Locate every blood parasite and identify its species.
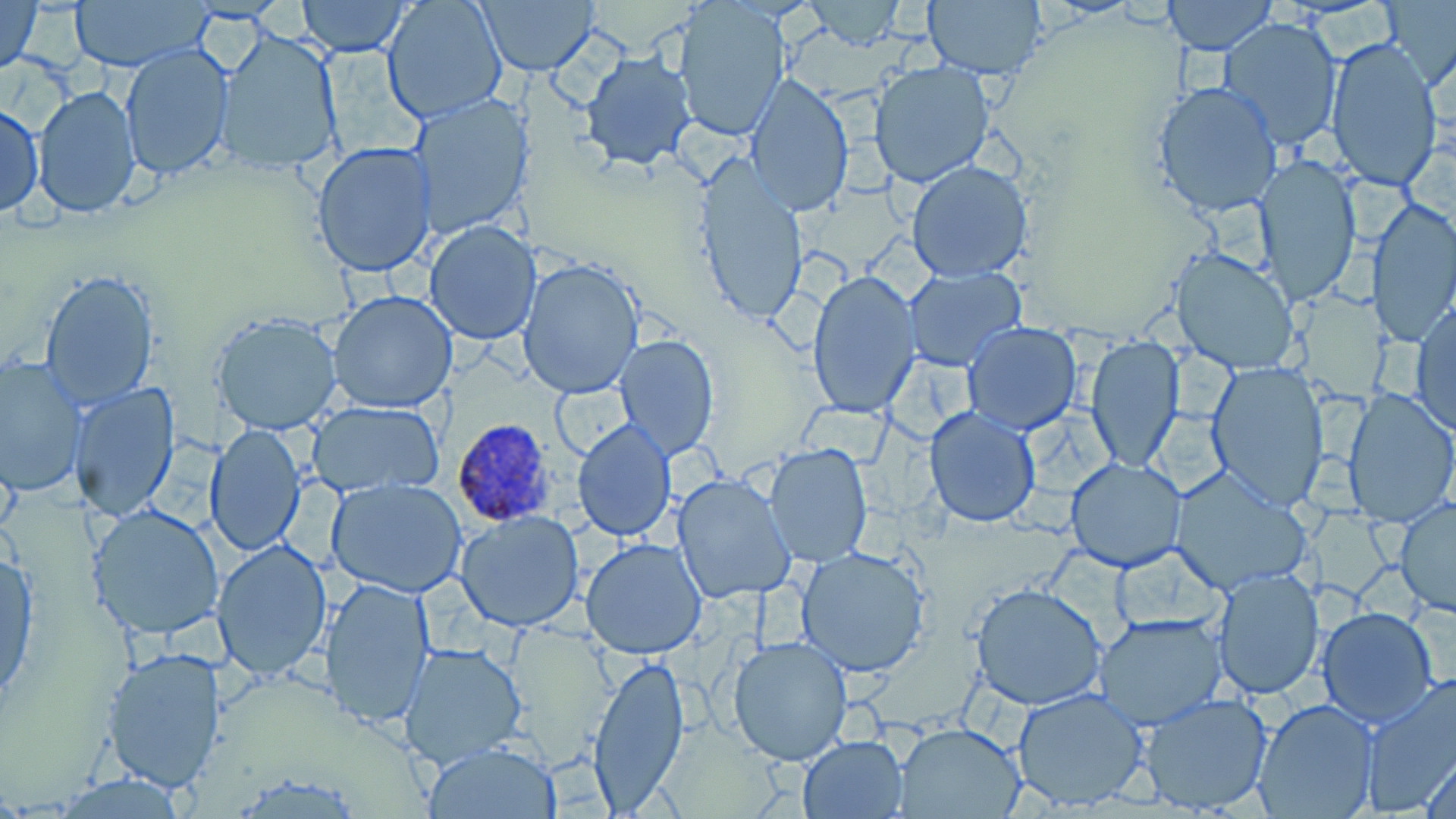
Approximate bounding boxes as (x1,y1)-(x2,y2) corner pairs in pixels.
Plasmodium ovale-infected red blood cells: (450,417)-(556,523).
No Plasmodium falciparum, Plasmodium malariae, Plasmodium vivax, Babesia divergens, or Trypanosoma brucei observed.

Summary:
  - Uninfected red blood cell locations: (0,0)-(45,76), (67,0)-(214,72), (295,0)-(412,56), (380,0)-(510,123), (795,0)-(916,53), (922,0)-(1048,82), (1164,0)-(1278,55), (477,1)-(600,78), (670,1)-(794,141), (1379,1)-(1456,87), (1214,16)-(1343,149), (216,29)-(343,176), (1324,37)-(1444,193), (119,43)-(233,178), (582,52)-(698,170), (870,61)-(995,187), (743,74)-(854,216), (1152,82)-(1284,220), (31,86)-(142,217), (410,95)-(534,239), (1,102)-(45,217), (310,142)-(438,277), (689,155)-(807,327), (1250,156)-(1363,304), (905,160)-(1034,281), (1367,195)-(1456,350), (426,220)-(541,346), (1171,247)-(1299,374), (517,259)-(645,400), (905,267)-(1025,370), (40,268)-(161,407), (808,270)-(921,419), (328,289)-(458,412), (1411,299)-(1456,437), (213,311)-(345,436), (962,322)-(1081,435), (614,333)-(719,459), (1085,337)-(1184,472), (0,356)-(85,498), (1205,361)-(1329,511), (70,383)-(181,523), (1340,388)-(1456,528), (306,400)-(445,495), (924,406)-(1041,528), (572,419)-(676,540), (206,423)-(307,557), (764,444)-(875,568), (1065,457)-(1186,572), (1169,467)-(1314,595), (671,473)-(797,606), (327,479)-(468,598), (1394,499)-(1456,614), (89,503)-(226,640), (454,511)-(586,630), (212,538)-(333,680), (581,538)-(709,660), (795,547)-(932,678), (0,548)-(39,711), (1212,569)-(1322,698), (319,577)-(436,727), (970,582)-(1107,710), (1318,607)-(1437,726), (1093,614)-(1228,728), (728,635)-(855,766), (401,642)-(529,768), (103,646)-(228,793), (588,654)-(690,810), (1360,673)-(1456,818), (1011,688)-(1151,810), (1138,691)-(1274,815), (1252,699)-(1379,818), (893,722)-(1024,816), (798,735)-(908,817), (424,741)-(563,818), (1422,745)-(1456,817), (52,774)-(194,816)
  - Slide-level diagnosis: Plasmodium ovale
  - Image size: 1456×819 pixels
  - Magnification: 1000x
  - Field of view: one of a larger specimen
  - Stain: May-Grünwald-Giemsa
  - Modality: optical microscopy
  - Preparation: thin blood film